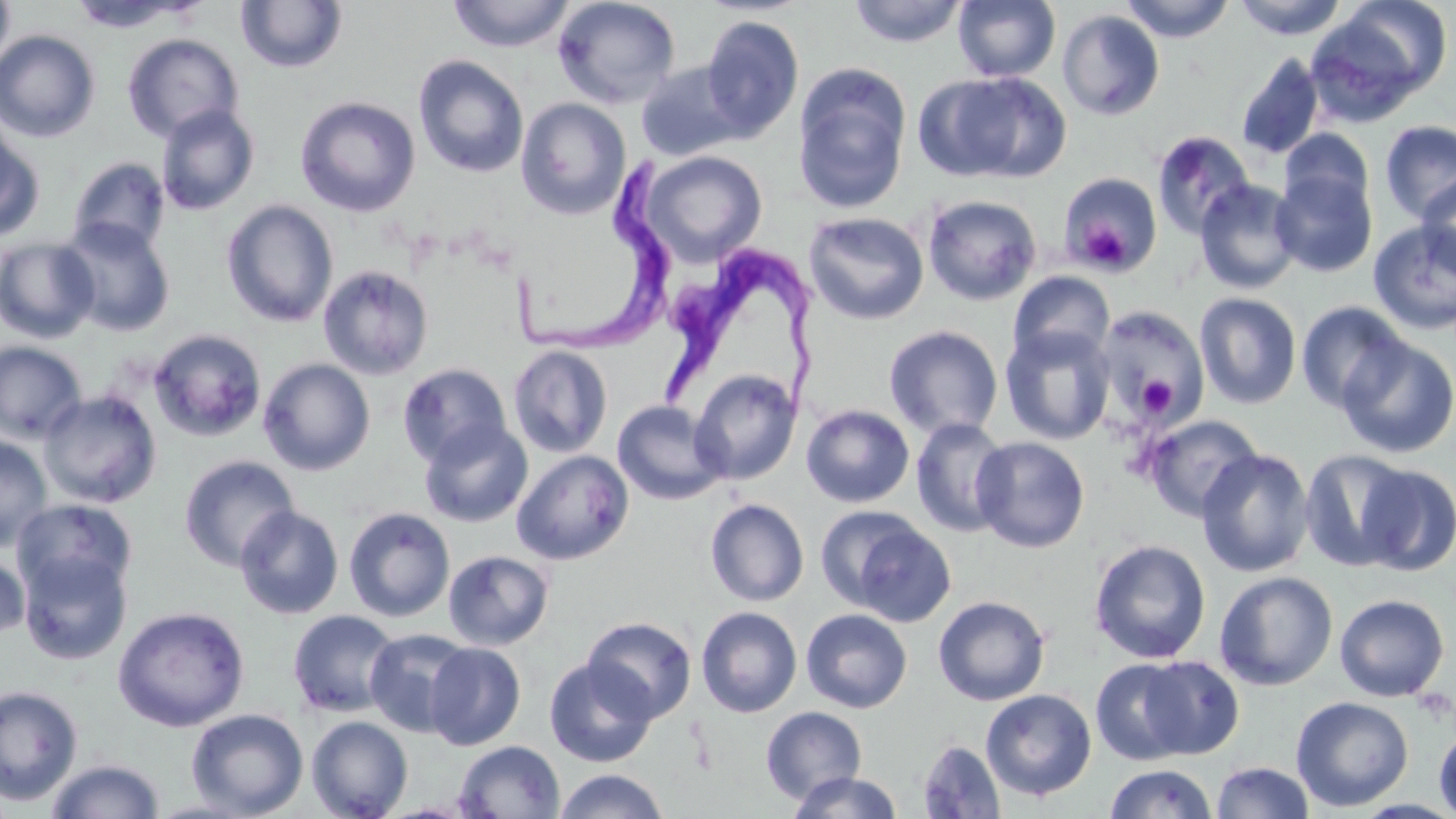
Summary:
  - Coordinate format: approximate bounding boxes as named x1/y1/x2/y2 corners in pixels
  - Platelet locations: (x1=1076, y1=219, x2=1131, y2=271), (x1=1135, y1=374, x2=1177, y2=417)
  - Trypanosoma brucei locations: (x1=505, y1=155, x2=676, y2=360), (x1=662, y1=243, x2=826, y2=414)
  - Uninfected red blood cell locations: (x1=0, y1=0, x2=15, y2=76), (x1=448, y1=0, x2=575, y2=52), (x1=552, y1=0, x2=681, y2=110), (x1=848, y1=0, x2=968, y2=47), (x1=953, y1=0, x2=1060, y2=82), (x1=1121, y1=0, x2=1236, y2=43), (x1=1232, y1=0, x2=1349, y2=39), (x1=1332, y1=0, x2=1454, y2=101), (x1=67, y1=1, x2=205, y2=34), (x1=236, y1=1, x2=348, y2=73), (x1=1057, y1=9, x2=1165, y2=121), (x1=700, y1=15, x2=804, y2=141), (x1=0, y1=29, x2=100, y2=142), (x1=122, y1=33, x2=244, y2=143), (x1=1236, y1=54, x2=1325, y2=160), (x1=413, y1=55, x2=529, y2=178), (x1=636, y1=62, x2=744, y2=162), (x1=793, y1=66, x2=911, y2=214), (x1=955, y1=73, x2=1072, y2=182), (x1=913, y1=74, x2=1027, y2=182), (x1=295, y1=96, x2=421, y2=217), (x1=516, y1=98, x2=631, y2=220), (x1=156, y1=104, x2=260, y2=215), (x1=1380, y1=120, x2=1456, y2=224), (x1=0, y1=121, x2=43, y2=243), (x1=1278, y1=128, x2=1375, y2=219), (x1=1151, y1=130, x2=1256, y2=239), (x1=640, y1=150, x2=768, y2=267), (x1=68, y1=156, x2=170, y2=256), (x1=1272, y1=169, x2=1377, y2=277), (x1=1059, y1=172, x2=1162, y2=277), (x1=1416, y1=174, x2=1456, y2=280), (x1=1195, y1=179, x2=1302, y2=294), (x1=921, y1=194, x2=1042, y2=306), (x1=221, y1=200, x2=339, y2=328), (x1=803, y1=211, x2=930, y2=325), (x1=57, y1=218, x2=175, y2=337), (x1=1367, y1=220, x2=1456, y2=336), (x1=0, y1=237, x2=100, y2=343), (x1=318, y1=264, x2=434, y2=380), (x1=1008, y1=271, x2=1115, y2=367), (x1=1195, y1=293, x2=1302, y2=409), (x1=1295, y1=301, x2=1411, y2=414), (x1=1094, y1=306, x2=1209, y2=427), (x1=884, y1=325, x2=1003, y2=440), (x1=1000, y1=327, x2=1115, y2=445), (x1=148, y1=328, x2=268, y2=442), (x1=1336, y1=336, x2=1456, y2=458), (x1=0, y1=341, x2=87, y2=444), (x1=508, y1=345, x2=612, y2=458), (x1=258, y1=358, x2=375, y2=475), (x1=398, y1=362, x2=512, y2=466), (x1=690, y1=369, x2=802, y2=485), (x1=38, y1=388, x2=162, y2=508), (x1=612, y1=400, x2=728, y2=505), (x1=801, y1=404, x2=915, y2=508), (x1=1143, y1=414, x2=1264, y2=522), (x1=910, y1=417, x2=1012, y2=538), (x1=419, y1=420, x2=533, y2=528), (x1=0, y1=435, x2=52, y2=551), (x1=971, y1=436, x2=1090, y2=553), (x1=1196, y1=448, x2=1314, y2=577), (x1=1299, y1=449, x2=1416, y2=572), (x1=511, y1=450, x2=634, y2=565), (x1=178, y1=455, x2=300, y2=571), (x1=1356, y1=463, x2=1456, y2=576), (x1=12, y1=498, x2=138, y2=602), (x1=705, y1=498, x2=810, y2=606), (x1=235, y1=505, x2=344, y2=619), (x1=343, y1=507, x2=455, y2=622), (x1=818, y1=507, x2=954, y2=624), (x1=1088, y1=539, x2=1211, y2=664), (x1=18, y1=548, x2=133, y2=665), (x1=443, y1=549, x2=554, y2=650), (x1=0, y1=551, x2=30, y2=641), (x1=1214, y1=571, x2=1338, y2=690), (x1=1334, y1=594, x2=1450, y2=702), (x1=933, y1=595, x2=1050, y2=706), (x1=112, y1=606, x2=250, y2=732), (x1=696, y1=606, x2=802, y2=717), (x1=801, y1=608, x2=912, y2=713), (x1=287, y1=609, x2=400, y2=718), (x1=582, y1=616, x2=697, y2=723), (x1=364, y1=629, x2=474, y2=737), (x1=424, y1=642, x2=526, y2=750), (x1=544, y1=657, x2=657, y2=767), (x1=1137, y1=657, x2=1246, y2=760), (x1=1091, y1=658, x2=1196, y2=766), (x1=0, y1=684, x2=83, y2=806), (x1=981, y1=689, x2=1096, y2=801), (x1=1290, y1=696, x2=1414, y2=812), (x1=760, y1=706, x2=867, y2=804), (x1=186, y1=708, x2=309, y2=817), (x1=306, y1=715, x2=413, y2=819), (x1=1433, y1=724, x2=1456, y2=819), (x1=917, y1=738, x2=1006, y2=819), (x1=453, y1=740, x2=565, y2=819), (x1=44, y1=758, x2=165, y2=819), (x1=1212, y1=761, x2=1315, y2=818), (x1=1105, y1=763, x2=1217, y2=819), (x1=553, y1=769, x2=670, y2=819), (x1=786, y1=770, x2=904, y2=819)
  - Slide-level diagnosis: Trypanosoma brucei
  - Field of view: single
  - Magnification: 1000x
  - Stain: May-Grünwald-Giemsa
  - Preparation: thin blood film
  - Modality: light microscopy
  - Image size: 1456×819 pixels